Assess this cell for malaria.
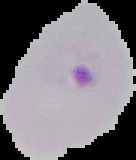
Parasitized.

Image is 136×160 pixels. From a thin blood smear. The area outside the segmented cell region is set to black.